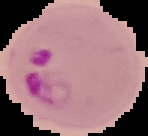
From a thin blood film. Result: malaria parasites identified. Segmented cell region on a black background. Image is 148×136 pixels.